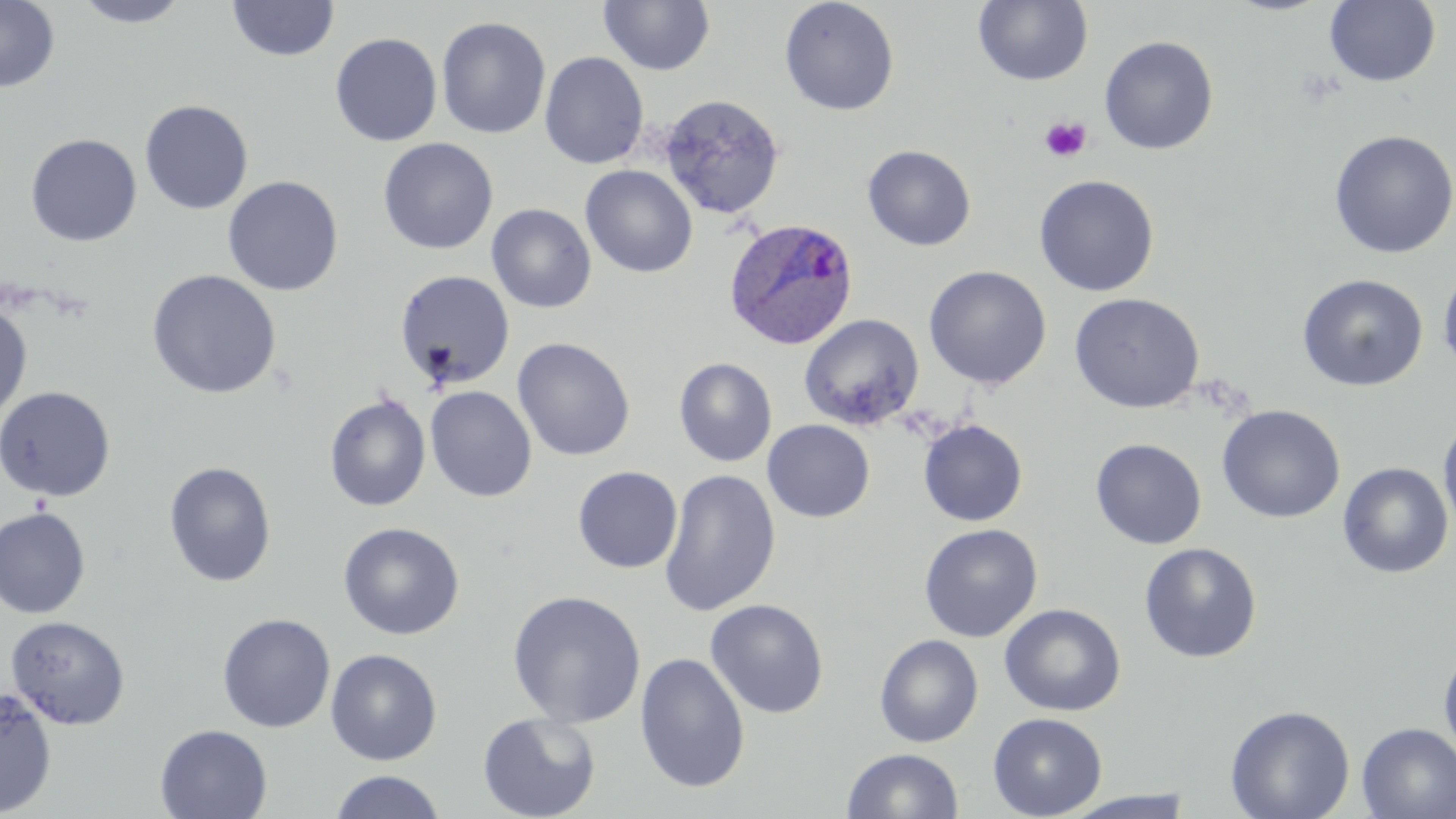
Approximate bounding boxes as named x1/y1/x2/y2 corners in pixels. Platelet locations: (x1=1039, y1=116, x2=1091, y2=163). Uninfected red blood cell locations: (x1=0, y1=0, x2=60, y2=92), (x1=72, y1=0, x2=191, y2=27), (x1=227, y1=0, x2=339, y2=62), (x1=599, y1=0, x2=715, y2=76), (x1=778, y1=0, x2=900, y2=116), (x1=973, y1=0, x2=1093, y2=86), (x1=1324, y1=0, x2=1440, y2=87), (x1=436, y1=16, x2=551, y2=139), (x1=330, y1=32, x2=442, y2=146), (x1=1099, y1=35, x2=1218, y2=154), (x1=539, y1=51, x2=649, y2=169), (x1=658, y1=93, x2=786, y2=220), (x1=139, y1=99, x2=254, y2=214), (x1=1329, y1=130, x2=1456, y2=258), (x1=25, y1=133, x2=142, y2=247), (x1=377, y1=137, x2=498, y2=254), (x1=862, y1=144, x2=976, y2=251), (x1=580, y1=164, x2=698, y2=278), (x1=1034, y1=174, x2=1159, y2=297), (x1=222, y1=175, x2=344, y2=296), (x1=486, y1=204, x2=596, y2=313), (x1=924, y1=265, x2=1052, y2=389), (x1=1438, y1=266, x2=1456, y2=375), (x1=146, y1=269, x2=282, y2=399), (x1=395, y1=269, x2=515, y2=391), (x1=1297, y1=273, x2=1429, y2=392), (x1=1069, y1=292, x2=1204, y2=413), (x1=0, y1=302, x2=33, y2=422), (x1=799, y1=313, x2=924, y2=430), (x1=512, y1=337, x2=635, y2=461), (x1=674, y1=358, x2=777, y2=467), (x1=0, y1=385, x2=116, y2=501), (x1=425, y1=386, x2=537, y2=502), (x1=324, y1=392, x2=431, y2=512), (x1=1217, y1=405, x2=1345, y2=523), (x1=1438, y1=413, x2=1456, y2=539), (x1=762, y1=419, x2=874, y2=522), (x1=918, y1=419, x2=1028, y2=526), (x1=1091, y1=438, x2=1207, y2=549), (x1=163, y1=461, x2=276, y2=587), (x1=1337, y1=462, x2=1454, y2=579), (x1=572, y1=466, x2=682, y2=573), (x1=659, y1=469, x2=781, y2=616), (x1=0, y1=507, x2=91, y2=619), (x1=338, y1=521, x2=465, y2=640), (x1=919, y1=523, x2=1042, y2=642), (x1=1139, y1=542, x2=1262, y2=662), (x1=507, y1=589, x2=646, y2=728), (x1=705, y1=598, x2=829, y2=718), (x1=999, y1=603, x2=1126, y2=716), (x1=216, y1=612, x2=335, y2=733), (x1=4, y1=614, x2=131, y2=730), (x1=874, y1=633, x2=983, y2=747), (x1=1438, y1=644, x2=1456, y2=765), (x1=325, y1=648, x2=443, y2=765), (x1=635, y1=652, x2=750, y2=793), (x1=0, y1=686, x2=57, y2=816), (x1=1225, y1=704, x2=1355, y2=819), (x1=477, y1=711, x2=601, y2=819), (x1=988, y1=712, x2=1107, y2=818), (x1=1356, y1=723, x2=1456, y2=818), (x1=154, y1=724, x2=272, y2=819), (x1=841, y1=748, x2=964, y2=819), (x1=328, y1=771, x2=447, y2=819), (x1=1061, y1=790, x2=1197, y2=818). Plasmodium ovale-infected red blood cell locations: (x1=723, y1=217, x2=859, y2=351). Slide-level diagnosis: Plasmodium ovale. Image is 1456×819 pixels. Single field of view. 1000x magnification. Optical microscopy. Thin blood smear. May-Grünwald-Giemsa-stained preparation.